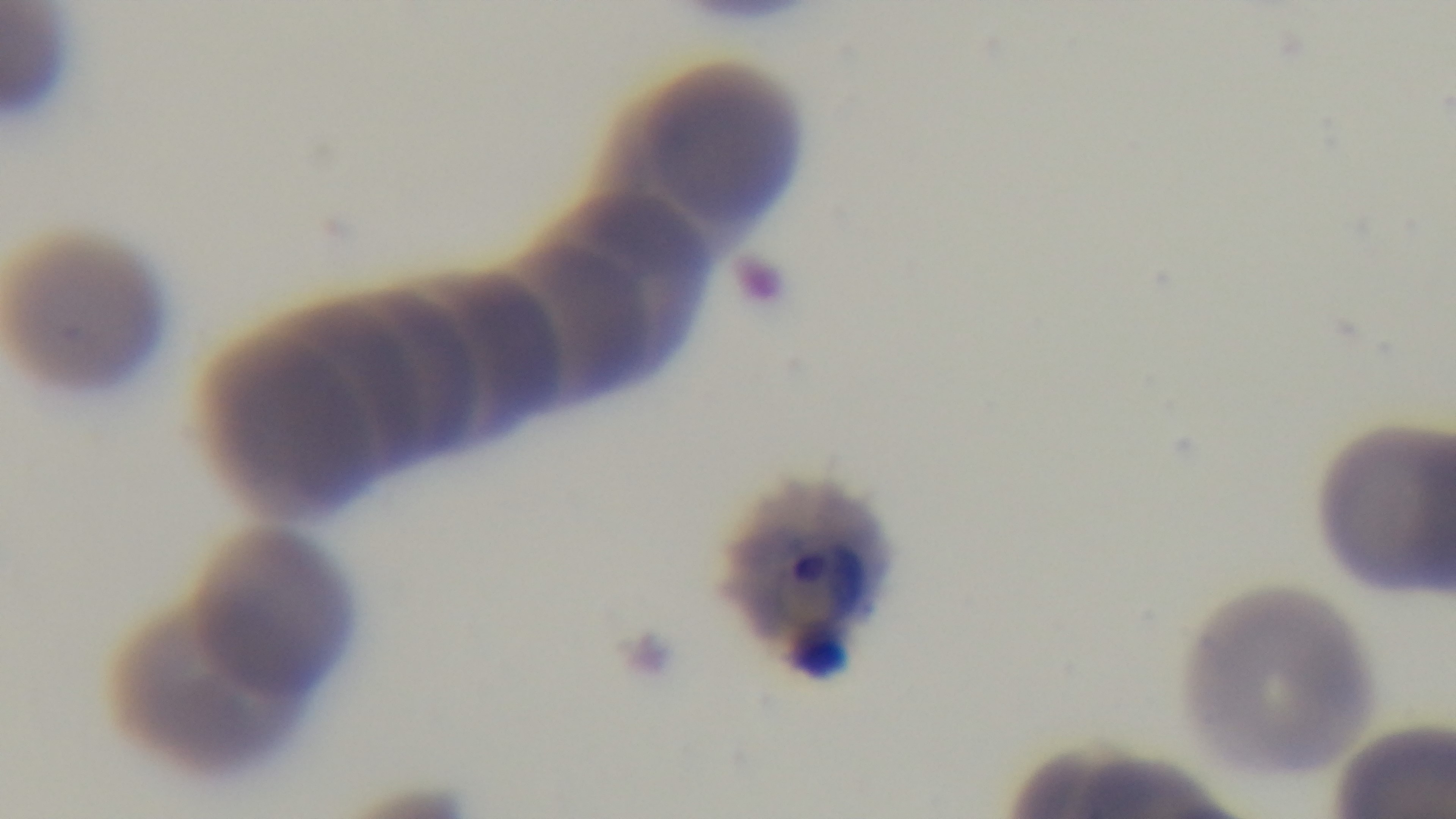
Summary:
  - Malaria status: positive
  - Field of view: one from the slide
  - Capture: mounted 4K digital camera
  - Modality: light microscopy
  - Preparation: thin
  - Objective: 100x oil immersion
  - Stain: Giemsa